Point out each Plasmodium parasite.
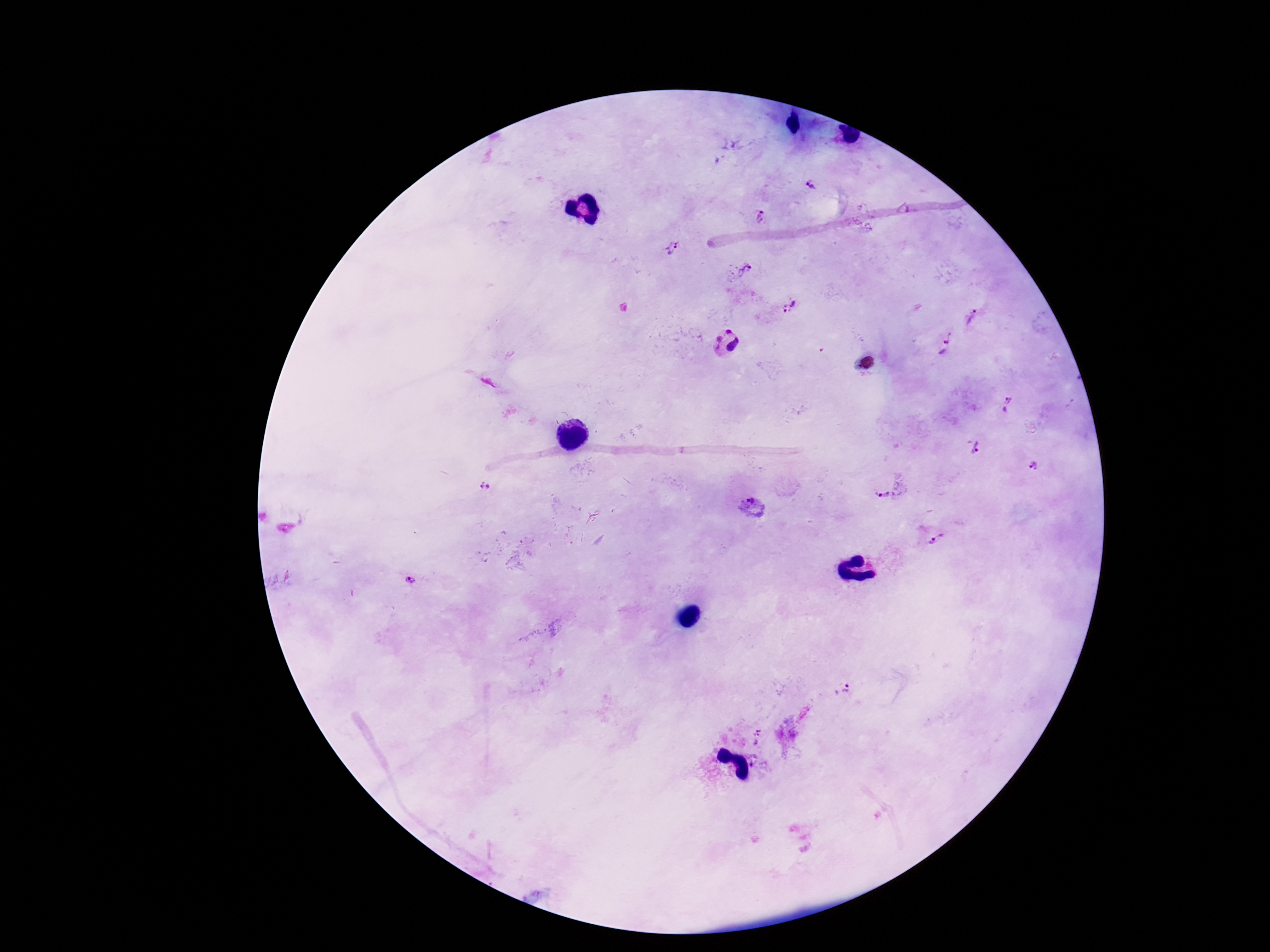
Approximate centers as {x, y} in pixels.
Plasmodium parasites: {811, 185}, {762, 216}, {673, 249}, {741, 271}, {792, 306}, {973, 317}, {726, 340}, {944, 341}, {1007, 405}, {973, 447}, {1034, 464}, {490, 487}, {884, 494}, {753, 506}, {937, 537}, {410, 581}, {845, 689}, {758, 736}, {755, 766}.

Patient malaria status: positive. Smartphone photograph taken through the microscope eyepiece. Giemsa stain. Thick blood film. Single field of view. 100x magnification. Image is 1270×952 pixels.